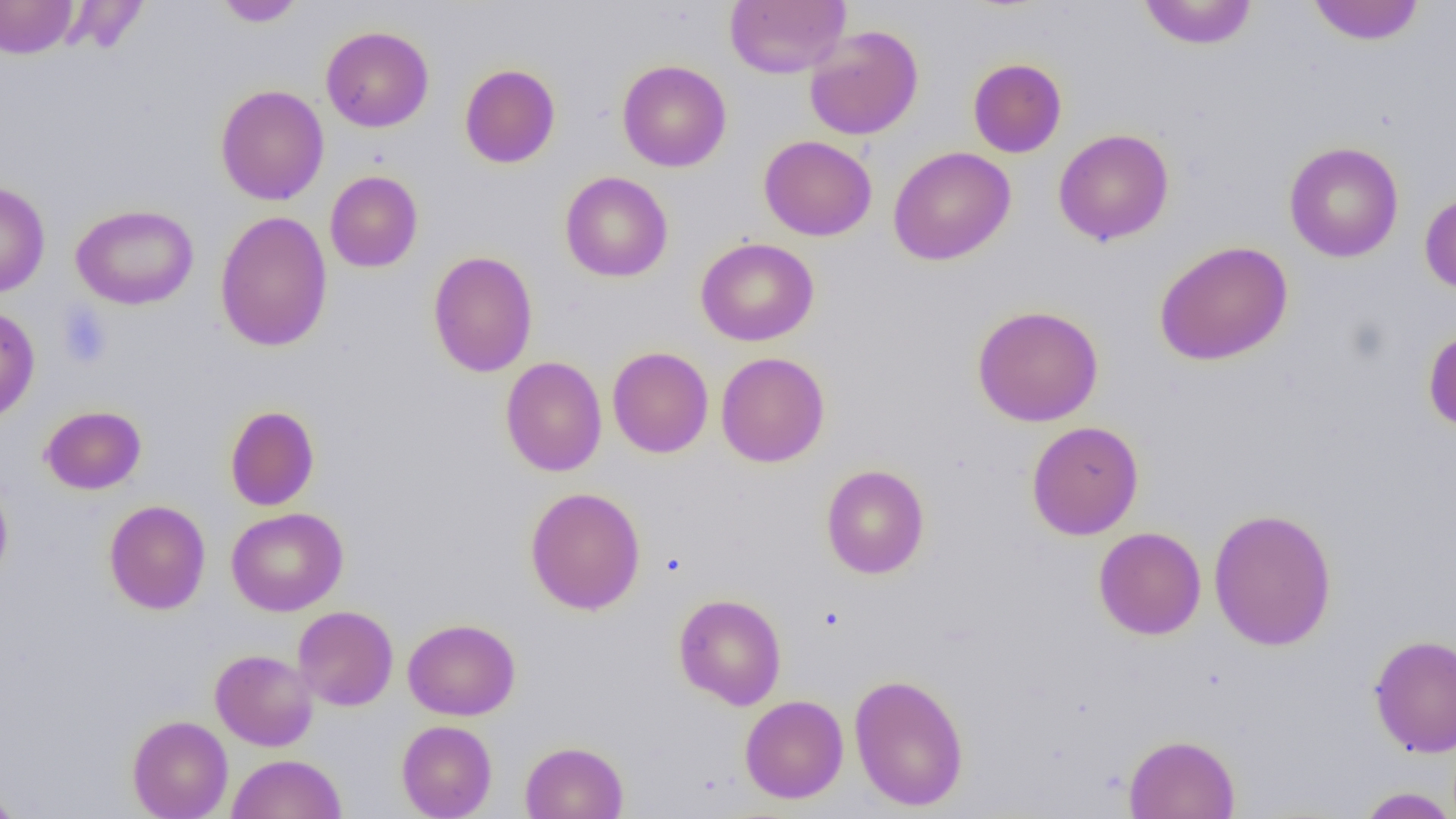

Summary:
  - Coordinate format: approximate bounding boxes as named x1/y1/x2/y2 corners in pixels
  - Uninfected red blood cell locations: (x1=214, y1=0, x2=305, y2=27), (x1=724, y1=0, x2=850, y2=78), (x1=0, y1=1, x2=79, y2=59), (x1=1138, y1=1, x2=1258, y2=50), (x1=1307, y1=1, x2=1425, y2=45), (x1=321, y1=25, x2=434, y2=132), (x1=804, y1=25, x2=923, y2=140), (x1=968, y1=57, x2=1067, y2=158), (x1=617, y1=59, x2=731, y2=172), (x1=459, y1=64, x2=561, y2=168), (x1=215, y1=84, x2=329, y2=205), (x1=1053, y1=128, x2=1174, y2=246), (x1=759, y1=135, x2=877, y2=241), (x1=1284, y1=142, x2=1403, y2=262), (x1=888, y1=146, x2=1015, y2=266), (x1=324, y1=170, x2=423, y2=272), (x1=560, y1=172, x2=673, y2=282), (x1=0, y1=181, x2=50, y2=297), (x1=1419, y1=191, x2=1456, y2=295), (x1=71, y1=203, x2=199, y2=310), (x1=215, y1=210, x2=333, y2=352), (x1=695, y1=237, x2=819, y2=346), (x1=1154, y1=240, x2=1293, y2=366), (x1=427, y1=250, x2=538, y2=377), (x1=972, y1=304, x2=1104, y2=427), (x1=0, y1=306, x2=40, y2=424), (x1=1423, y1=326, x2=1456, y2=432), (x1=607, y1=346, x2=713, y2=458), (x1=715, y1=352, x2=830, y2=468), (x1=500, y1=357, x2=608, y2=476), (x1=40, y1=405, x2=146, y2=494), (x1=224, y1=405, x2=320, y2=511), (x1=1026, y1=421, x2=1144, y2=540), (x1=820, y1=464, x2=930, y2=579), (x1=0, y1=476, x2=13, y2=586), (x1=524, y1=486, x2=646, y2=615), (x1=104, y1=499, x2=211, y2=615), (x1=226, y1=507, x2=348, y2=616), (x1=1208, y1=507, x2=1337, y2=651), (x1=1094, y1=526, x2=1207, y2=640), (x1=673, y1=593, x2=787, y2=709), (x1=293, y1=605, x2=398, y2=711), (x1=403, y1=618, x2=520, y2=720), (x1=1369, y1=633, x2=1456, y2=757), (x1=210, y1=649, x2=318, y2=751), (x1=849, y1=673, x2=969, y2=811), (x1=740, y1=694, x2=849, y2=803), (x1=127, y1=715, x2=233, y2=819), (x1=396, y1=719, x2=497, y2=819), (x1=1123, y1=733, x2=1240, y2=818), (x1=520, y1=741, x2=628, y2=819), (x1=228, y1=753, x2=347, y2=819), (x1=0, y1=782, x2=22, y2=819), (x1=1354, y1=786, x2=1456, y2=818)
  - Platelet locations: (x1=57, y1=303, x2=113, y2=369)
  - Slide-level diagnosis: negative for blood parasites
  - Field of view: single
  - Image size: 1456×819 pixels
  - Preparation: thin blood film
  - Magnification: 1000x
  - Modality: optical microscopy